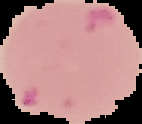

Result: malaria parasites detected. From a thin blood film. Image is 142×124 pixels. Segmented cell region on a black background.